State which parasite is depicted.
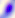

Toxoplasma gondii.

Summary:
  - Magnification: 400x
  - Modality: micrograph